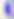

modality = photomicrograph
identification = Toxoplasma gondii
magnification = 400x